Name the parasite shown.
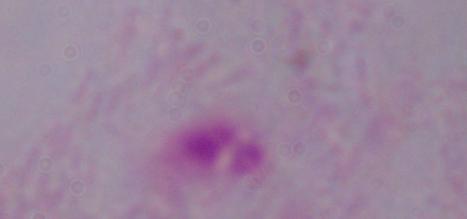
This is a trichomonad.

Photomicrograph. 1000x magnification.